Point out each Plasmodium parasite.
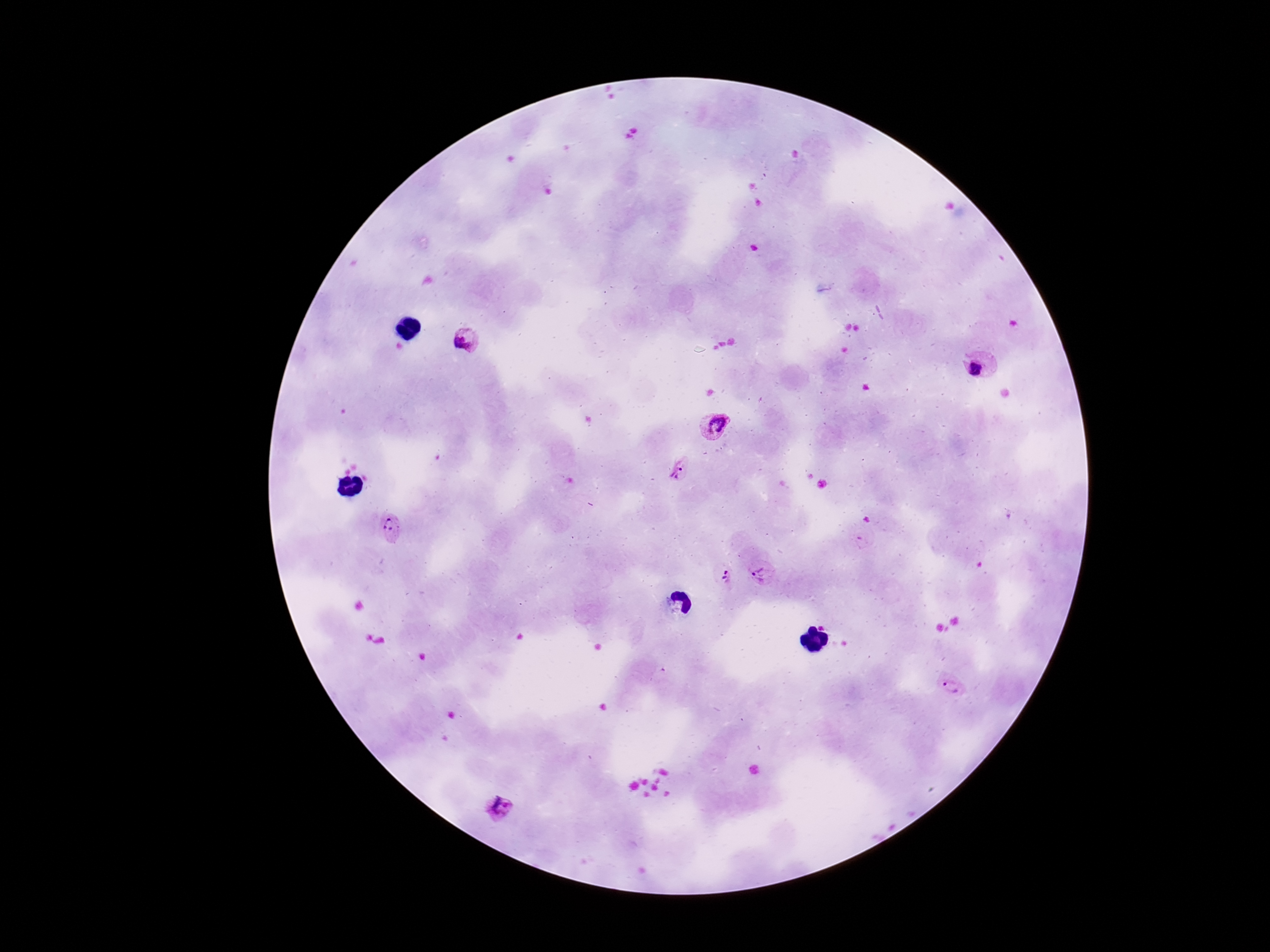

Approximate centers as [x, y] in pixels.
Plasmodium parasites: [466, 338], [980, 368], [715, 424], [679, 469], [394, 528], [764, 570], [725, 578], [952, 688], [500, 810].

Summary:
  - Magnification: 100x
  - Stain: Giemsa
  - Preparation: thick blood smear
  - Capture: smartphone camera through the microscope eyepiece
  - Patient malaria status: infected
  - Field of view: single
  - Image size: 1270×952 pixels